Classify this cell by malaria status.
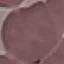

It is uninfected.

Giemsa stain. Photographed with a smartphone camera at the microscope eyepiece. Thin blood smear. Cell patch, automatically extracted from a larger field of view and resized to 64 × 64 pixels.